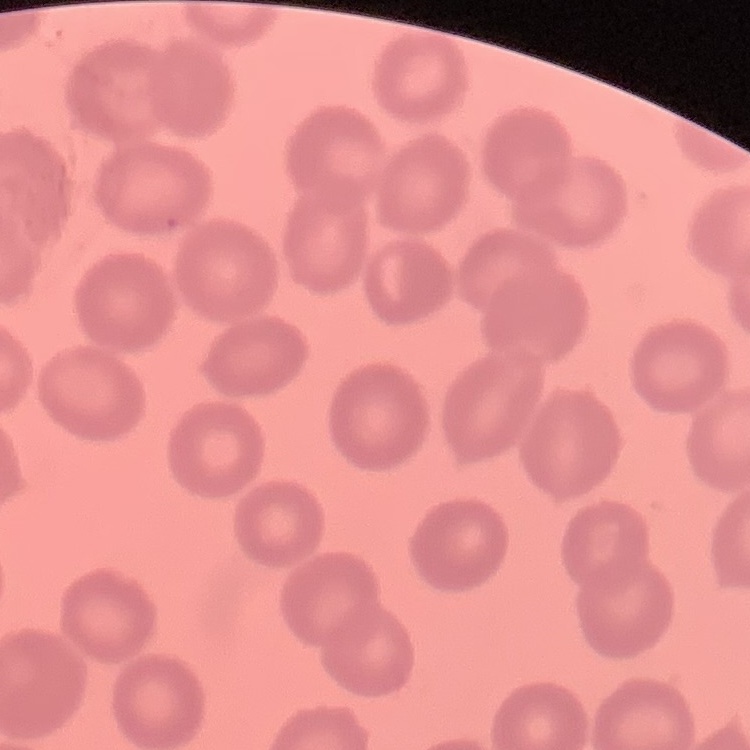

{
  "erythrocyte_morphology": "no rouleaux formation",
  "preparation": "thin blood film",
  "image_type": "square crop of a larger photomicrograph",
  "stain": "Field's or Giemsa"
}